Outline each blood parasite and name the species.
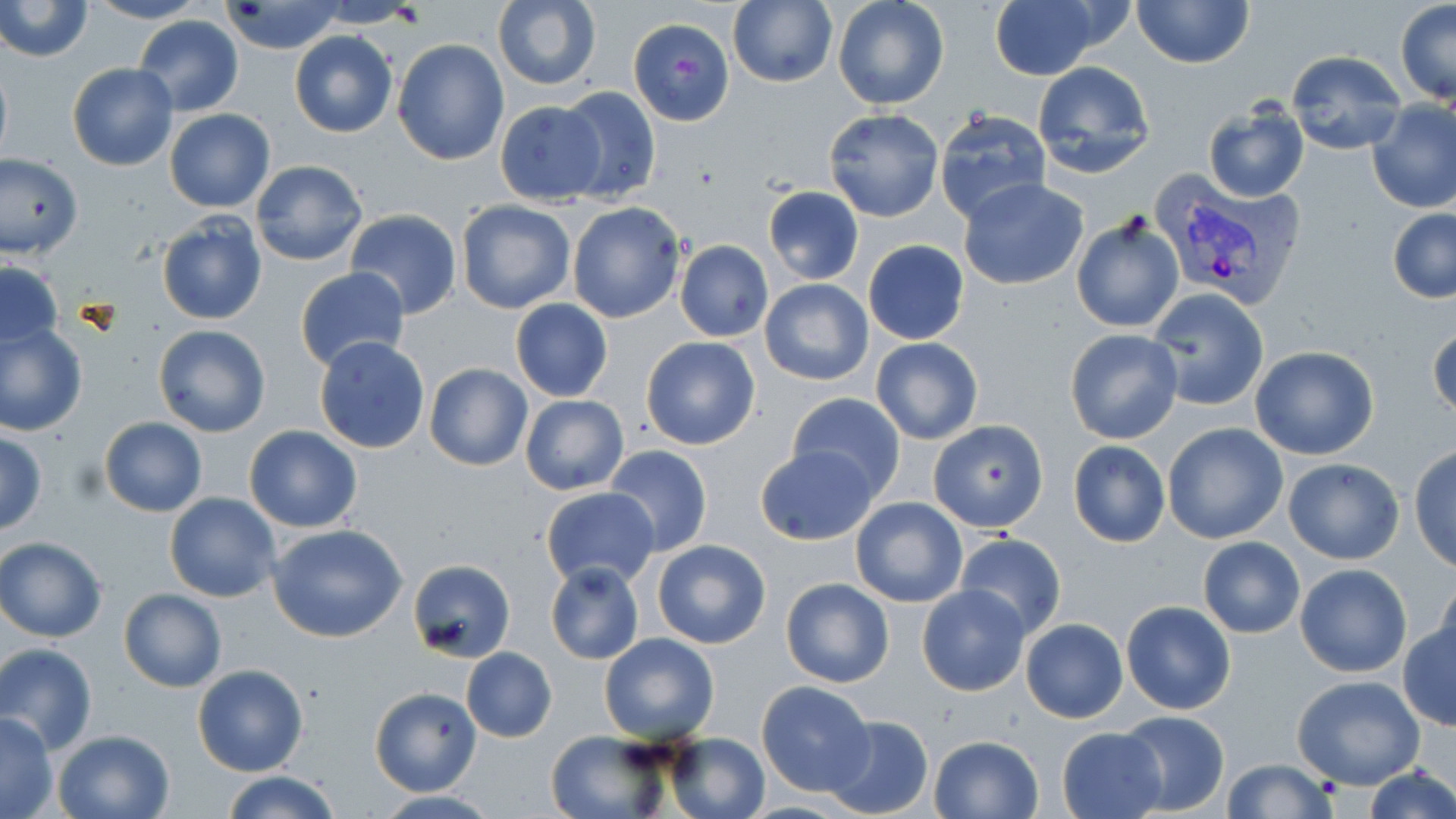

Approximate bounding boxes as (x1, y1, x2, y2) in pixels.
Plasmodium vivax-infected red blood cells: (1155, 174, 1308, 311).
No Plasmodium falciparum, Plasmodium ovale, Plasmodium malariae, Babesia divergens, or Trypanosoma brucei observed.

slide-level diagnosis = Plasmodium vivax
field of view = one of a larger specimen
magnification = 1000x
image size = 1456×819 pixels
modality = light microscopy
preparation = thin blood film
uninfected red blood cell locations = approximate bounding boxes as (x1, y1, x2, y2) in pixels: (0, 0, 93, 62), (85, 0, 206, 24), (832, 0, 950, 109), (989, 0, 1101, 81), (1132, 0, 1254, 69), (312, 1, 423, 27), (492, 1, 601, 90), (1395, 1, 1456, 106), (219, 2, 346, 54), (726, 2, 838, 88), (133, 16, 244, 116), (628, 18, 735, 126), (290, 29, 397, 137), (391, 38, 509, 165), (1286, 51, 1406, 154), (0, 54, 12, 172), (1029, 61, 1157, 179), (67, 63, 177, 171), (555, 85, 662, 205), (494, 100, 607, 205), (1367, 101, 1456, 215), (1202, 104, 1310, 202), (823, 107, 943, 223), (934, 108, 1052, 224), (164, 109, 275, 212), (0, 155, 82, 259), (251, 159, 368, 266), (958, 177, 1089, 290), (764, 184, 864, 286), (455, 199, 576, 314), (566, 201, 685, 324), (1388, 207, 1456, 304), (346, 209, 463, 320), (155, 212, 268, 326), (1070, 212, 1185, 334), (863, 238, 970, 345), (675, 240, 773, 341), (2, 260, 63, 356), (294, 267, 410, 374), (759, 278, 874, 385), (1147, 288, 1270, 411), (511, 297, 613, 402), (0, 321, 88, 436), (153, 324, 271, 437), (1429, 326, 1456, 421), (1063, 328, 1184, 446), (313, 337, 431, 454), (641, 337, 761, 450), (871, 337, 983, 445), (1249, 345, 1380, 461), (424, 363, 532, 471), (785, 393, 909, 500), (519, 394, 630, 495), (98, 417, 207, 517), (928, 418, 1049, 533), (1162, 421, 1289, 544), (244, 426, 362, 531), (0, 430, 49, 536), (1065, 439, 1171, 548), (754, 444, 878, 546), (604, 445, 712, 558), (1409, 446, 1456, 572), (1282, 458, 1404, 565), (541, 485, 660, 589), (165, 491, 282, 602), (849, 495, 968, 608), (268, 525, 408, 643), (954, 533, 1068, 642), (0, 538, 107, 641), (651, 538, 772, 648), (1197, 538, 1305, 638), (407, 560, 515, 663), (545, 561, 645, 664), (1295, 563, 1412, 677), (1430, 572, 1456, 666), (780, 577, 894, 688), (916, 584, 1032, 697), (119, 588, 227, 693), (1121, 600, 1235, 714), (1020, 618, 1127, 722), (1399, 618, 1456, 729), (599, 632, 719, 743), (1, 644, 98, 753), (461, 647, 557, 743), (192, 664, 308, 776), (1292, 674, 1425, 789), (755, 679, 876, 795), (369, 686, 482, 796), (1116, 708, 1230, 816), (0, 711, 59, 818), (823, 713, 934, 818), (1057, 727, 1166, 818), (53, 728, 176, 819), (545, 730, 670, 818), (665, 733, 771, 819), (928, 734, 1045, 819), (1221, 758, 1339, 818), (1361, 765, 1454, 819), (218, 771, 344, 819), (366, 792, 505, 818)
stain = May-Grünwald-Giemsa